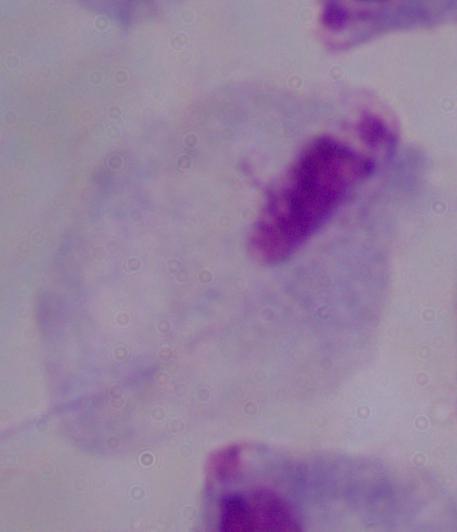

identification: trichomonad
modality: micrograph
magnification: 1000x